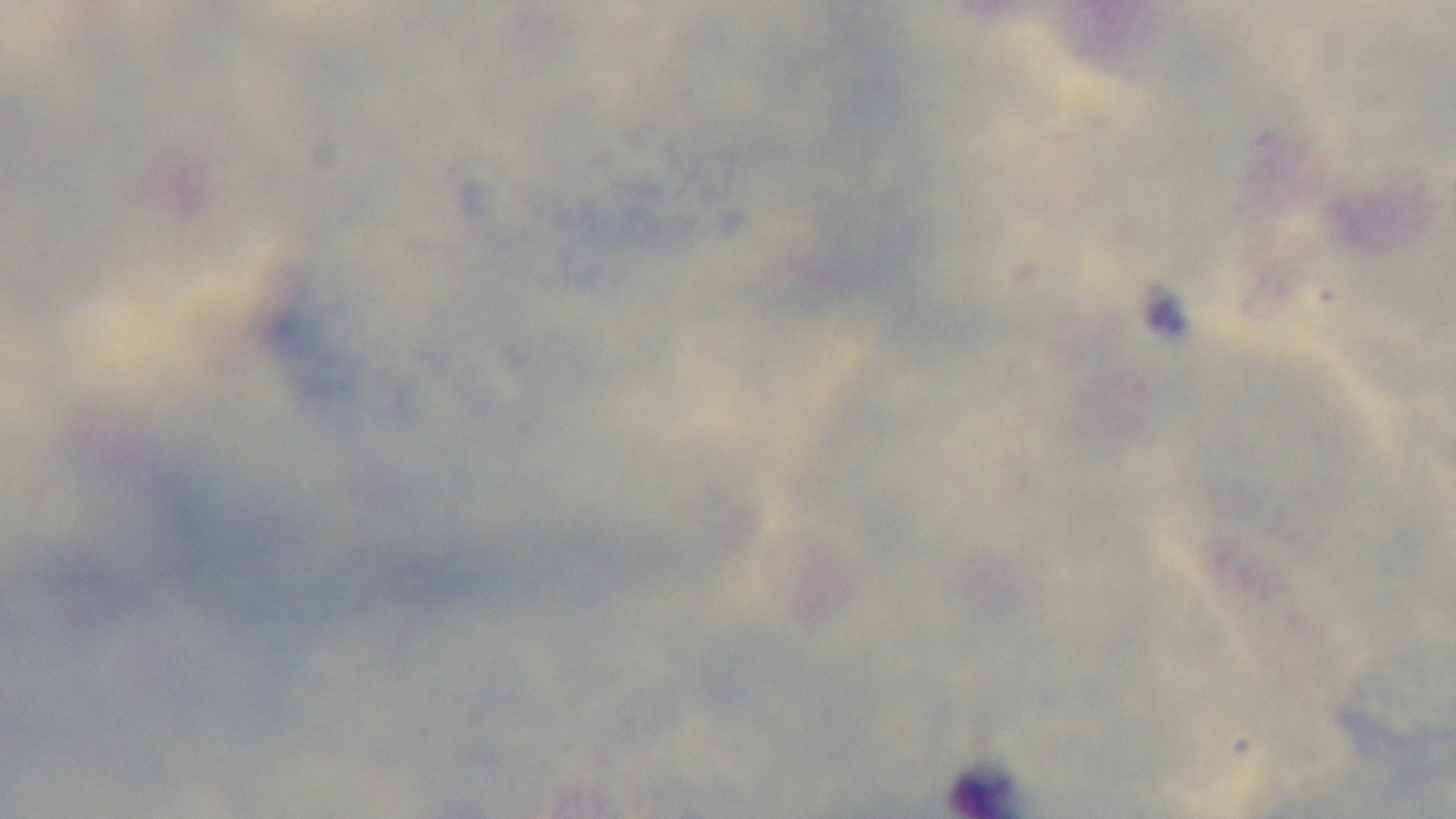
Summary:
  - Preparation: thick
  - Modality: light microscopy
  - Objective: 100x oil immersion
  - Stain: Giemsa
  - Capture: mounted 4K digital camera
  - Field of view: single
  - Malaria status: negative